Comment on the morphology of the erythrocytes.
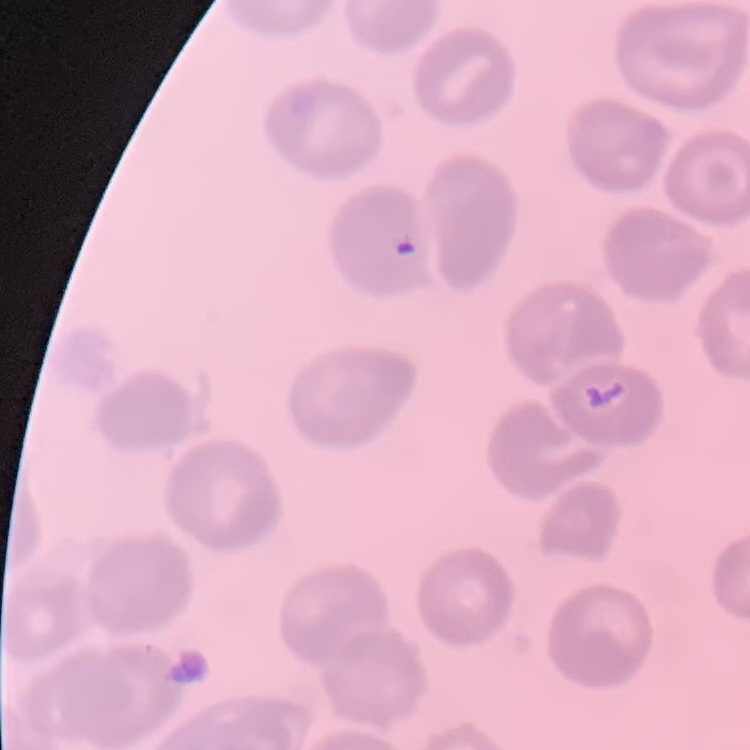
No rouleaux formation.

Summary:
  - Image type: square crop of a larger photomicrograph
  - Stain: Field's or Giemsa
  - Preparation: thin blood film